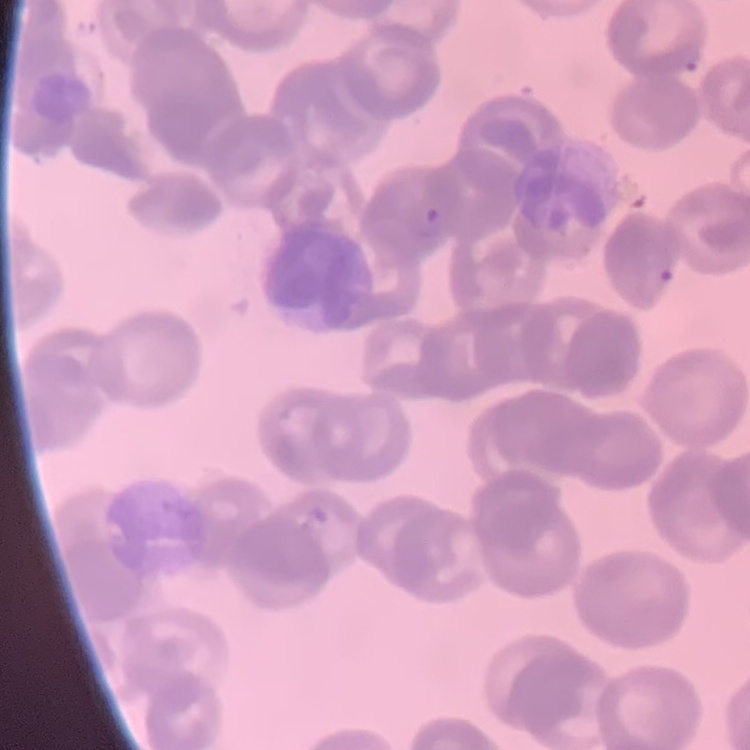
The erythrocytes exhibit rouleaux formation. Thin blood smear. Field's or Giemsa stain. Square crop of a larger photomicrograph.